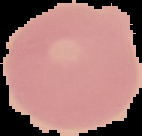

Cell region segmented out of the field of view; the surrounding area is masked to black. Malaria status: uninfected. From a thin blood film. Image is 142×136 pixels.